State which parasite is depicted.
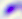

This is Toxoplasma gondii.

Summary:
  - Magnification: 400x
  - Modality: photomicrograph